Assess the background quality.
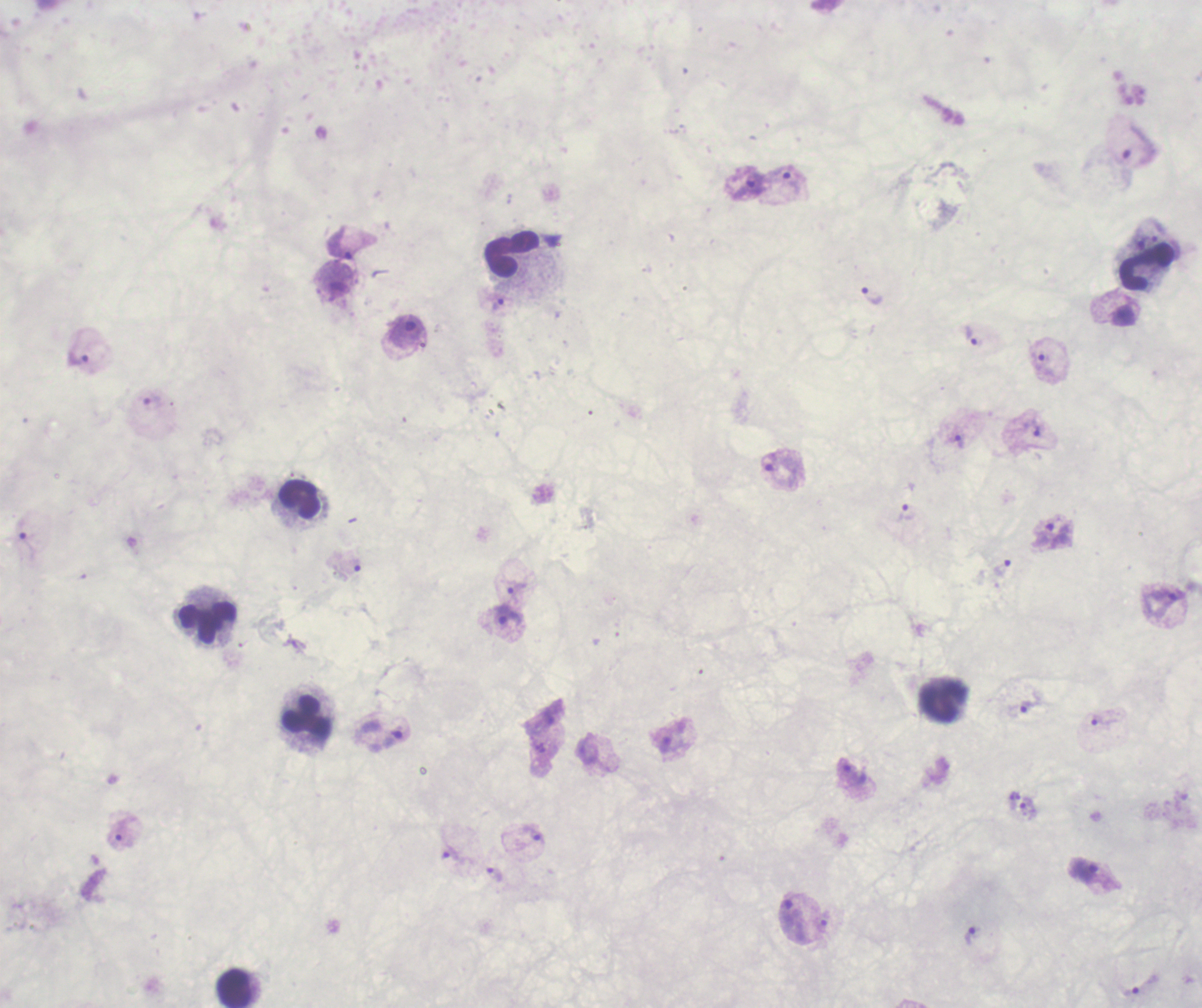
It is poor.

coordinate format = approximate centers as (x, y) in pixels
trophozoite locations = (1138, 143), (787, 179), (747, 183), (339, 245), (872, 296), (496, 304), (406, 330), (973, 337), (76, 360), (1043, 366), (150, 402), (1032, 429), (956, 440), (782, 472), (906, 512), (26, 536), (1052, 536), (1001, 567), (517, 591), (1166, 604), (505, 618), (1025, 709), (1106, 720), (391, 738), (669, 742), (852, 773), (1021, 804), (534, 835), (450, 856), (1085, 871), (495, 874), (793, 924), (970, 936), (1135, 985)
leukocyte locations = (511, 253), (1147, 267), (298, 500), (206, 621), (944, 698), (305, 717), (233, 988)
result = malaria parasites detected
preparation = thick blood film
stain = Romanowsky
magnification = 100x
field of view = single
image size = 1202×1008 pixels
context = previously used in a real diagnosis